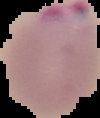
Summary:
  - Preparation: thin blood smear
  - Image size: 100×118 pixels
  - Image type: segmented cell region with the area outside set to black
  - Result: malaria parasites detected